Assess this cell for malaria.
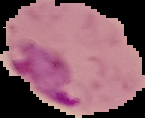

It is parasitized.

image size = 145×118 pixels
image type = segmented cell region with the area outside set to black
preparation = thin blood film